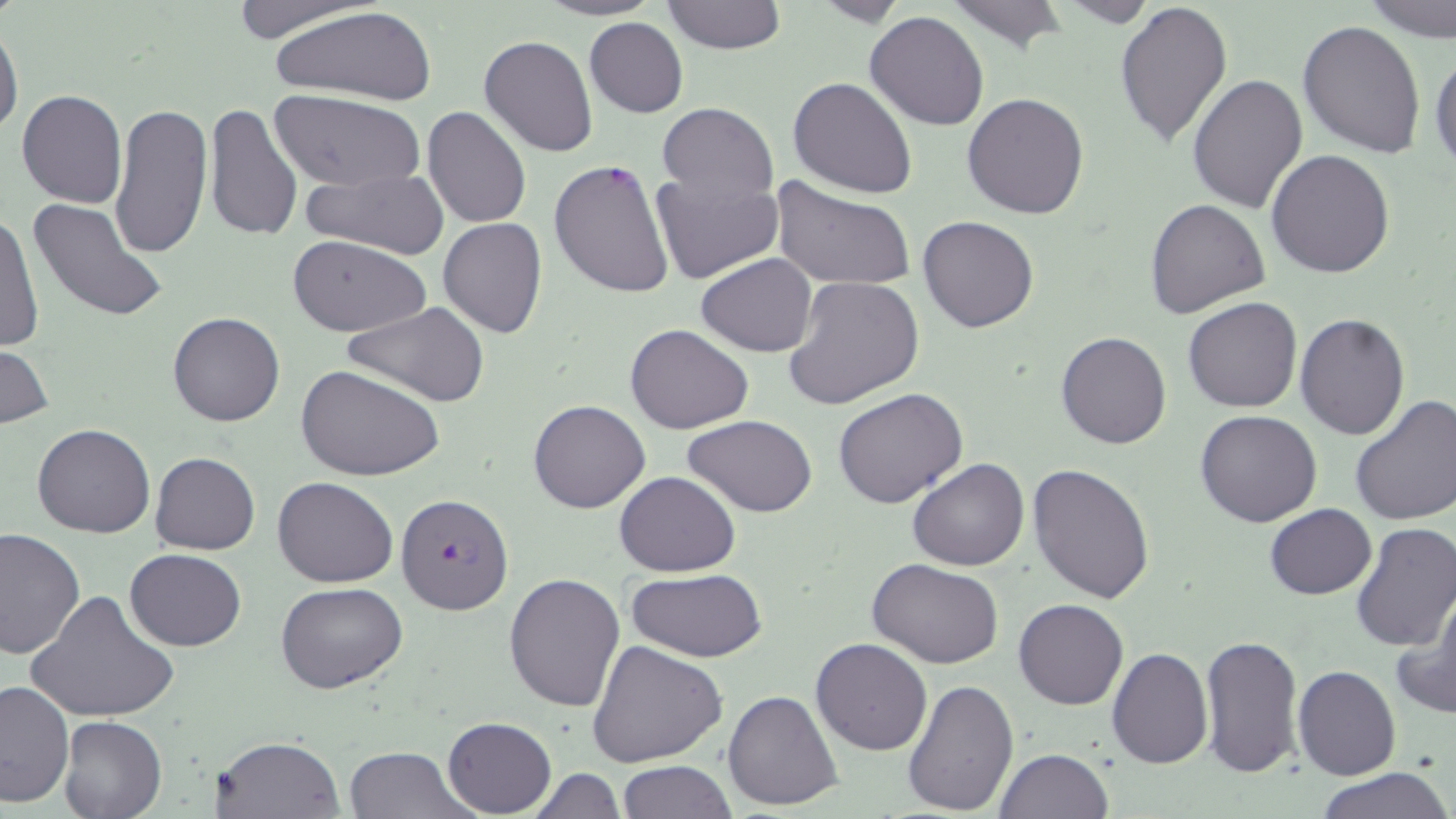

slide-level diagnosis = Plasmodium falciparum
magnification = 1000x
modality = light microscopy
preparation = thin blood film
uninfected red blood cell locations = approximate bounding boxes as [x1, y1, x2, y2] in pixels: [225, 0, 381, 43], [536, 0, 663, 20], [663, 0, 787, 53], [1052, 0, 1159, 27], [1113, 0, 1234, 149], [1357, 0, 1454, 39], [944, 1, 1070, 52], [266, 5, 441, 110], [865, 12, 990, 130], [584, 17, 689, 118], [1297, 19, 1426, 158], [0, 24, 23, 139], [479, 34, 599, 157], [1430, 48, 1455, 172], [1187, 73, 1308, 215], [788, 76, 918, 200], [17, 90, 128, 209], [270, 93, 422, 192], [962, 93, 1090, 219], [107, 102, 212, 261], [203, 102, 304, 243], [657, 103, 778, 205], [423, 105, 531, 229], [1266, 148, 1396, 279], [549, 159, 674, 301], [301, 167, 449, 259], [649, 169, 783, 285], [770, 177, 917, 292], [1145, 198, 1269, 317], [26, 199, 167, 324], [1, 208, 43, 355], [917, 215, 1039, 333], [437, 217, 548, 339], [286, 234, 433, 337], [697, 253, 817, 356], [783, 276, 925, 410], [1183, 296, 1303, 413], [342, 302, 491, 409], [167, 311, 285, 427], [1295, 314, 1410, 440], [625, 323, 754, 434], [1056, 331, 1172, 450], [1, 340, 55, 431], [297, 364, 445, 480], [832, 388, 968, 510], [1350, 394, 1456, 526], [528, 399, 650, 514], [1195, 409, 1324, 528], [684, 415, 818, 517], [32, 422, 155, 538], [150, 451, 260, 555], [907, 458, 1031, 571], [1026, 461, 1157, 605], [614, 471, 739, 576], [272, 477, 398, 587], [1264, 503, 1377, 599], [1351, 523, 1456, 652], [0, 526, 85, 659], [124, 548, 248, 651], [867, 559, 1005, 670], [625, 569, 769, 662], [503, 572, 628, 711], [275, 580, 407, 693], [27, 589, 181, 726], [1394, 589, 1456, 720], [1014, 598, 1128, 710], [1200, 634, 1304, 778], [809, 638, 932, 756], [588, 639, 728, 768], [1106, 646, 1213, 768], [1294, 665, 1401, 780], [901, 677, 1018, 817], [1, 679, 76, 809], [723, 689, 845, 811], [59, 715, 166, 819], [442, 716, 555, 816], [213, 734, 345, 818], [341, 745, 475, 819], [993, 749, 1113, 819], [617, 760, 736, 818], [528, 767, 626, 819], [1314, 767, 1451, 819]
Plasmodium falciparum-infected red blood cell locations = approximate bounding boxes as [x1, y1, x2, y2] in pixels: [395, 493, 514, 616]
stain = May-Grünwald-Giemsa
field of view = one of a larger specimen
image size = 1456×819 pixels